Classify this cell by malaria status.
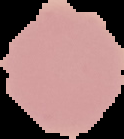
Uninfected.

Segmented cell region on a black background. Image is 124×139 pixels. From a thin blood film.